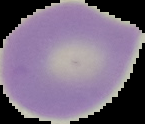

preparation = thin blood smear
image type = segmented cell region on a black background
image size = 145×124 pixels
malaria status = uninfected